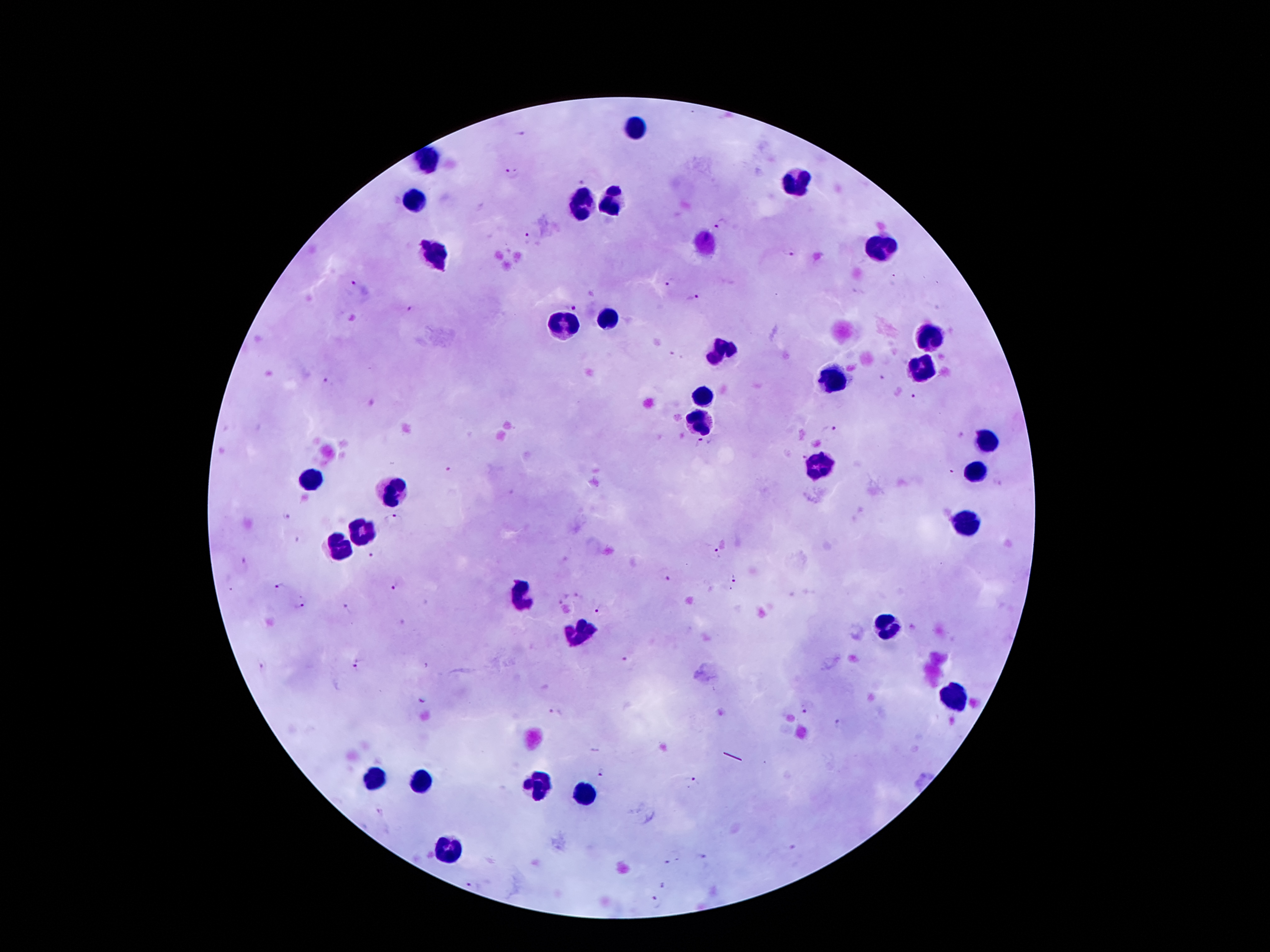
Approximate centers as {x, y} in pixels. Leukocyte locations: {637, 127}, {434, 164}, {796, 181}, {417, 203}, {613, 203}, {583, 207}, {704, 241}, {882, 246}, {436, 255}, {613, 317}, {562, 326}, {926, 341}, {723, 352}, {921, 373}, {831, 384}, {704, 399}, {699, 423}, {986, 446}, {822, 465}, {977, 474}, {312, 483}, {391, 496}, {964, 524}, {356, 530}, {339, 548}, {528, 599}, {885, 626}, {585, 630}, {952, 695}, {375, 781}, {423, 783}, {538, 784}, {587, 793}, {444, 853}. Plasmodium parasite locations: {520, 134}, {512, 175}, {585, 181}, {722, 225}, {530, 238}, {791, 252}, {670, 283}, {354, 284}, {695, 300}, {573, 303}, {410, 310}, {883, 378}, {326, 386}, {917, 399}, {831, 429}, {699, 444}, {800, 454}, {449, 469}, {951, 475}, {287, 517}, {393, 519}, {302, 540}, {376, 552}, {716, 553}, {240, 564}, {664, 574}, {734, 576}, {399, 584}, {278, 588}, {563, 598}, {300, 607}, {348, 609}, {600, 609}, {628, 658}, {358, 666}, {263, 668}, {423, 696}, {807, 709}, {556, 713}, {839, 726}, {603, 774}, {693, 783}, {792, 848}, {701, 859}, {672, 860}, {668, 886}, {655, 902}. One field from this slide. Smartphone photograph taken through the microscope eyepiece. Patient malaria status: infected with Plasmodium falciparum. Image is 1270×952 pixels. 100x magnification. Giemsa-stained preparation. Thick peripheral-blood smear.